Report the malaria status of this cell.
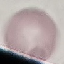
Uninfected.

Summary:
  - Capture: smartphone camera at the microscope eyepiece
  - Image type: automatically extracted cell patch, resized to 64 × 64 pixels
  - Preparation: thin blood film
  - Stain: Giemsa